Locate every Plasmodium parasite and identify its life-cycle stage.
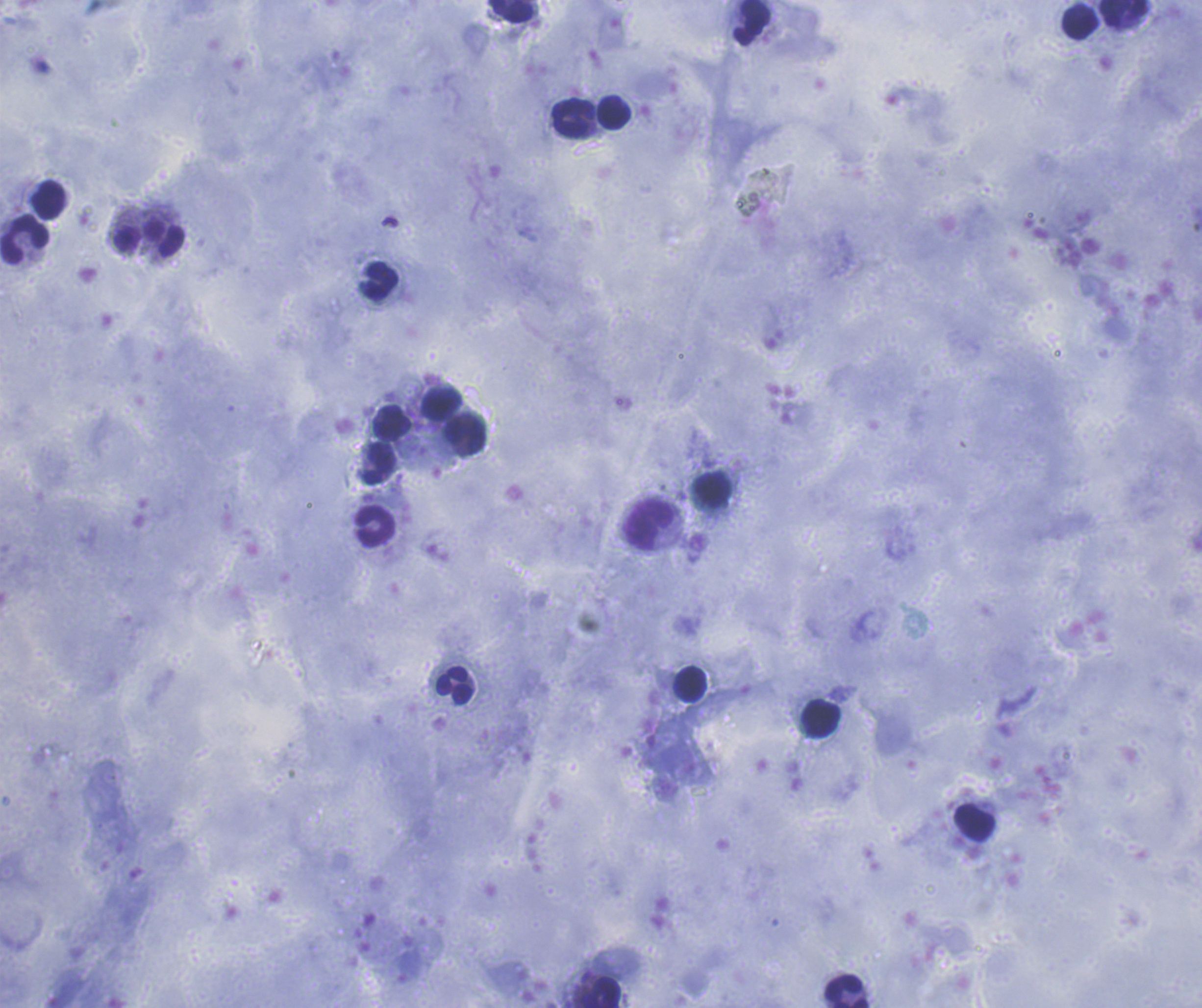

No Plasmodium parasites seen.

coordinate format = approximate centers as [x, y] in pixels
leukocyte locations = [512, 12], [1123, 14], [751, 23], [1079, 24], [613, 111], [574, 119], [48, 200], [149, 238], [24, 239], [378, 282], [443, 405], [393, 422], [468, 436], [378, 462], [714, 490], [650, 524], [374, 525], [690, 684], [454, 686], [821, 718], [975, 824], [847, 991], [603, 994]
image size = 1202×1008 pixels
preparation = thick blood film
context = previously used in an actual diagnosis
field of view = single
magnification = 100x
background quality = satisfactory
coloration quality = good
stain = Romanowsky